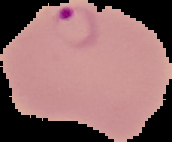
From a thin blood film. Segmented cell region on a black background. Result: malaria parasites detected. Image is 172×142 pixels.